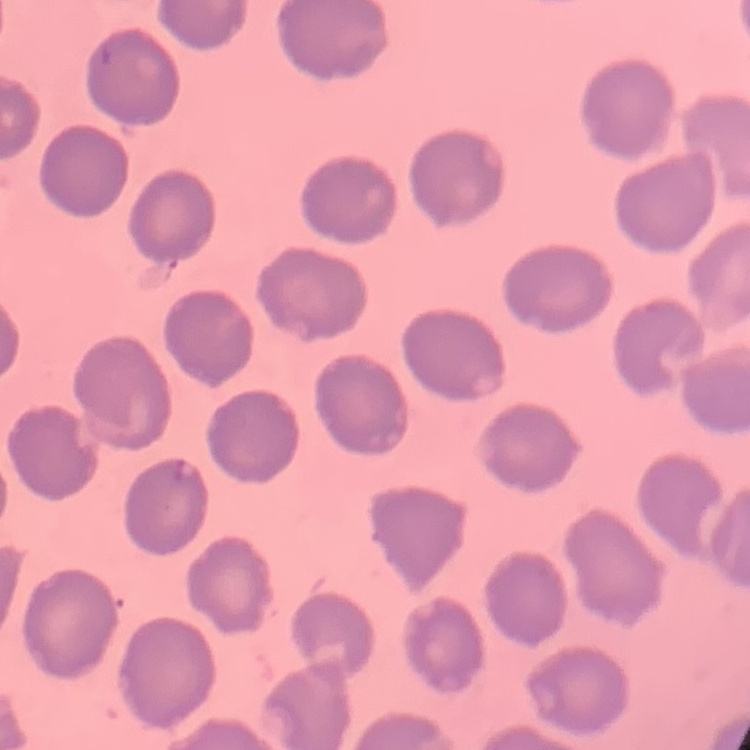
Summary:
  - Red blood cell morphology: no rouleaux formation
  - Preparation: thin peripheral smear
  - Image type: one tile cut from a larger photomicrograph
  - Stain: Field's or Giemsa